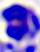
Summary:
  - Modality: photomicrograph
  - Identification: white blood cell
  - Magnification: 400x